Report the malaria status.
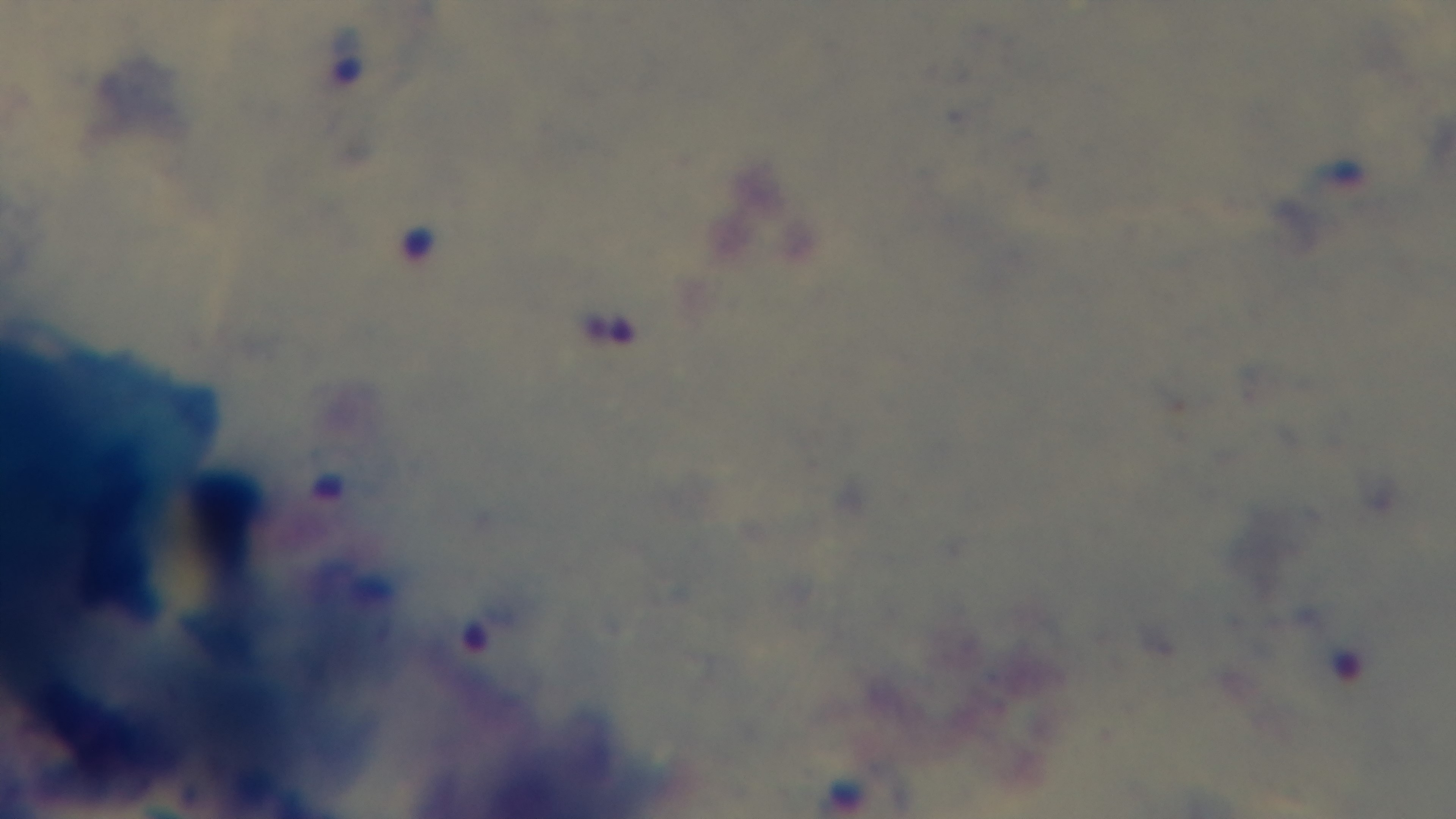
It is infected.

Mounted 4K digital camera. One field from the slide. Giemsa stain. 100x oil-immersion objective. Preparation: thick blood film. Light microscopy.